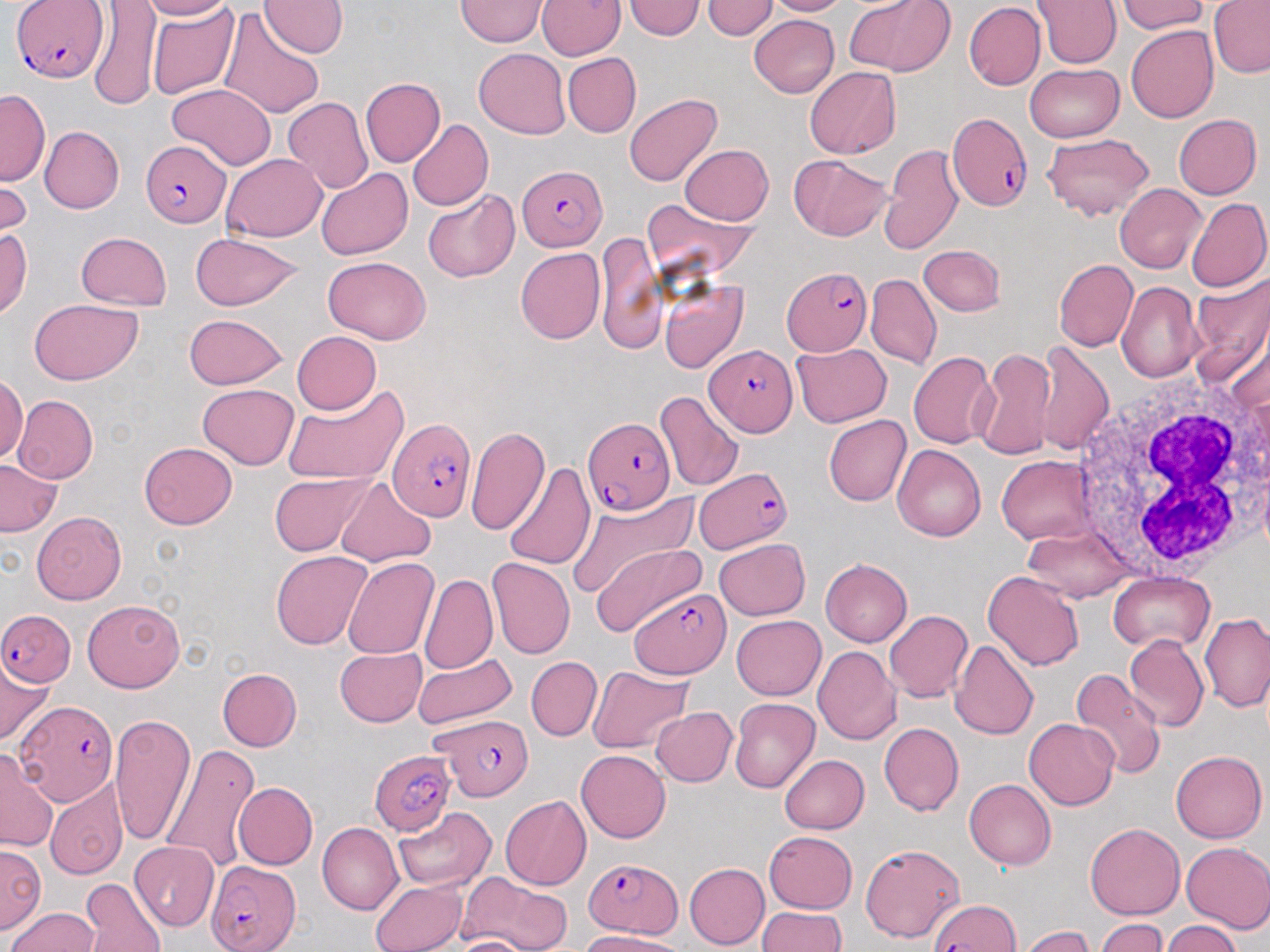
Approximate bounding boxes as named x1/y1/x2/y2 corners in pixels. Uninfected red blood cell locations: (x1=136, y1=0, x2=234, y2=20), (x1=259, y1=0, x2=348, y2=58), (x1=537, y1=0, x2=625, y2=59), (x1=702, y1=0, x2=776, y2=39), (x1=762, y1=0, x2=848, y2=15), (x1=848, y1=0, x2=952, y2=75), (x1=1031, y1=0, x2=1122, y2=69), (x1=88, y1=1, x2=161, y2=108), (x1=455, y1=1, x2=549, y2=47), (x1=623, y1=1, x2=705, y2=39), (x1=1114, y1=1, x2=1209, y2=34), (x1=1208, y1=1, x2=1270, y2=78), (x1=964, y1=2, x2=1045, y2=89), (x1=148, y1=4, x2=242, y2=100), (x1=218, y1=7, x2=324, y2=120), (x1=749, y1=15, x2=839, y2=97), (x1=1125, y1=26, x2=1218, y2=123), (x1=474, y1=49, x2=569, y2=138), (x1=562, y1=53, x2=640, y2=137), (x1=1024, y1=63, x2=1125, y2=142), (x1=804, y1=68, x2=900, y2=159), (x1=359, y1=78, x2=445, y2=167), (x1=167, y1=82, x2=277, y2=170), (x1=0, y1=89, x2=50, y2=186), (x1=624, y1=94, x2=723, y2=186), (x1=282, y1=97, x2=373, y2=195), (x1=1174, y1=114, x2=1262, y2=199), (x1=407, y1=119, x2=493, y2=211), (x1=40, y1=126, x2=124, y2=214), (x1=1042, y1=132, x2=1153, y2=221), (x1=679, y1=145, x2=773, y2=225), (x1=879, y1=145, x2=963, y2=255), (x1=219, y1=153, x2=327, y2=241), (x1=790, y1=154, x2=891, y2=240), (x1=0, y1=164, x2=29, y2=243), (x1=315, y1=167, x2=412, y2=260), (x1=1115, y1=182, x2=1207, y2=274), (x1=422, y1=189, x2=520, y2=282), (x1=1185, y1=196, x2=1269, y2=292), (x1=642, y1=198, x2=757, y2=284), (x1=0, y1=227, x2=32, y2=320), (x1=76, y1=231, x2=171, y2=310), (x1=189, y1=232, x2=306, y2=312), (x1=595, y1=235, x2=665, y2=355), (x1=918, y1=245, x2=1005, y2=315), (x1=515, y1=247, x2=605, y2=344), (x1=322, y1=256, x2=431, y2=343), (x1=1054, y1=259, x2=1138, y2=351), (x1=1189, y1=271, x2=1270, y2=385), (x1=865, y1=273, x2=941, y2=369), (x1=658, y1=278, x2=747, y2=373), (x1=1116, y1=281, x2=1203, y2=383), (x1=28, y1=299, x2=142, y2=385), (x1=185, y1=314, x2=288, y2=388), (x1=1231, y1=321, x2=1270, y2=422), (x1=292, y1=331, x2=381, y2=414), (x1=1033, y1=342, x2=1113, y2=455), (x1=791, y1=343, x2=892, y2=427), (x1=973, y1=347, x2=1057, y2=461), (x1=908, y1=352, x2=998, y2=449), (x1=1, y1=375, x2=28, y2=464), (x1=282, y1=382, x2=409, y2=487), (x1=197, y1=383, x2=298, y2=469), (x1=654, y1=389, x2=744, y2=494), (x1=13, y1=395, x2=98, y2=483), (x1=824, y1=415, x2=910, y2=506), (x1=465, y1=425, x2=549, y2=535), (x1=138, y1=442, x2=237, y2=529), (x1=892, y1=444, x2=985, y2=542), (x1=996, y1=455, x2=1097, y2=545), (x1=0, y1=459, x2=62, y2=536), (x1=503, y1=461, x2=594, y2=569), (x1=269, y1=472, x2=372, y2=556), (x1=335, y1=478, x2=435, y2=566), (x1=567, y1=492, x2=698, y2=602), (x1=32, y1=511, x2=126, y2=605), (x1=1020, y1=526, x2=1134, y2=603), (x1=714, y1=538, x2=810, y2=621), (x1=590, y1=540, x2=705, y2=636), (x1=271, y1=551, x2=374, y2=650), (x1=342, y1=556, x2=438, y2=659), (x1=487, y1=557, x2=574, y2=659), (x1=820, y1=558, x2=912, y2=647), (x1=982, y1=570, x2=1084, y2=671), (x1=1108, y1=571, x2=1215, y2=652), (x1=417, y1=573, x2=497, y2=674), (x1=83, y1=599, x2=184, y2=693), (x1=884, y1=610, x2=973, y2=701), (x1=1200, y1=613, x2=1269, y2=712), (x1=732, y1=615, x2=826, y2=700), (x1=1123, y1=634, x2=1208, y2=733), (x1=949, y1=639, x2=1039, y2=740), (x1=812, y1=646, x2=902, y2=745), (x1=334, y1=648, x2=426, y2=727), (x1=413, y1=654, x2=517, y2=731), (x1=0, y1=656, x2=52, y2=746), (x1=527, y1=657, x2=602, y2=740), (x1=587, y1=665, x2=693, y2=754), (x1=216, y1=668, x2=301, y2=751), (x1=1069, y1=669, x2=1166, y2=781), (x1=730, y1=697, x2=819, y2=793), (x1=651, y1=707, x2=737, y2=786), (x1=110, y1=714, x2=195, y2=848), (x1=1024, y1=718, x2=1119, y2=811), (x1=879, y1=722, x2=965, y2=816), (x1=161, y1=745, x2=260, y2=873), (x1=0, y1=748, x2=59, y2=853), (x1=1170, y1=749, x2=1267, y2=843), (x1=576, y1=750, x2=671, y2=843), (x1=779, y1=755, x2=869, y2=834), (x1=964, y1=778, x2=1056, y2=869), (x1=45, y1=779, x2=128, y2=880), (x1=233, y1=782, x2=317, y2=869), (x1=500, y1=796, x2=590, y2=890), (x1=393, y1=808, x2=497, y2=891), (x1=1085, y1=822, x2=1185, y2=920), (x1=318, y1=823, x2=403, y2=915), (x1=764, y1=832, x2=857, y2=913), (x1=130, y1=842, x2=218, y2=931), (x1=1181, y1=842, x2=1270, y2=933), (x1=1, y1=843, x2=46, y2=933), (x1=861, y1=843, x2=965, y2=944), (x1=684, y1=862, x2=769, y2=950), (x1=459, y1=872, x2=572, y2=952), (x1=81, y1=879, x2=165, y2=950), (x1=370, y1=879, x2=466, y2=952), (x1=757, y1=906, x2=846, y2=952), (x1=7, y1=907, x2=100, y2=950), (x1=1095, y1=918, x2=1169, y2=952), (x1=1163, y1=920, x2=1242, y2=952), (x1=1019, y1=926, x2=1094, y2=952), (x1=580, y1=931, x2=683, y2=952), (x1=448, y1=935, x2=538, y2=952). Plasmodium falciparum-infected red blood cell locations: (x1=10, y1=1, x2=107, y2=82), (x1=946, y1=113, x2=1032, y2=211), (x1=141, y1=142, x2=226, y2=224), (x1=516, y1=165, x2=606, y2=250), (x1=782, y1=264, x2=871, y2=356), (x1=705, y1=344, x2=798, y2=436), (x1=390, y1=418, x2=476, y2=519), (x1=582, y1=418, x2=676, y2=518), (x1=693, y1=467, x2=792, y2=553), (x1=630, y1=588, x2=731, y2=679), (x1=3, y1=608, x2=74, y2=685), (x1=17, y1=700, x2=117, y2=803), (x1=434, y1=710, x2=534, y2=795), (x1=368, y1=751, x2=459, y2=835), (x1=585, y1=858, x2=682, y2=936), (x1=204, y1=861, x2=300, y2=951), (x1=929, y1=899, x2=1019, y2=951). White blood cell locations: (x1=1069, y1=374, x2=1270, y2=577). Slide-level diagnosis: Plasmodium falciparum. May-Grünwald-Giemsa stain. Light microscopy. Image is 1270×952 pixels. Single field of view. Thin blood smear. 1000x magnification.